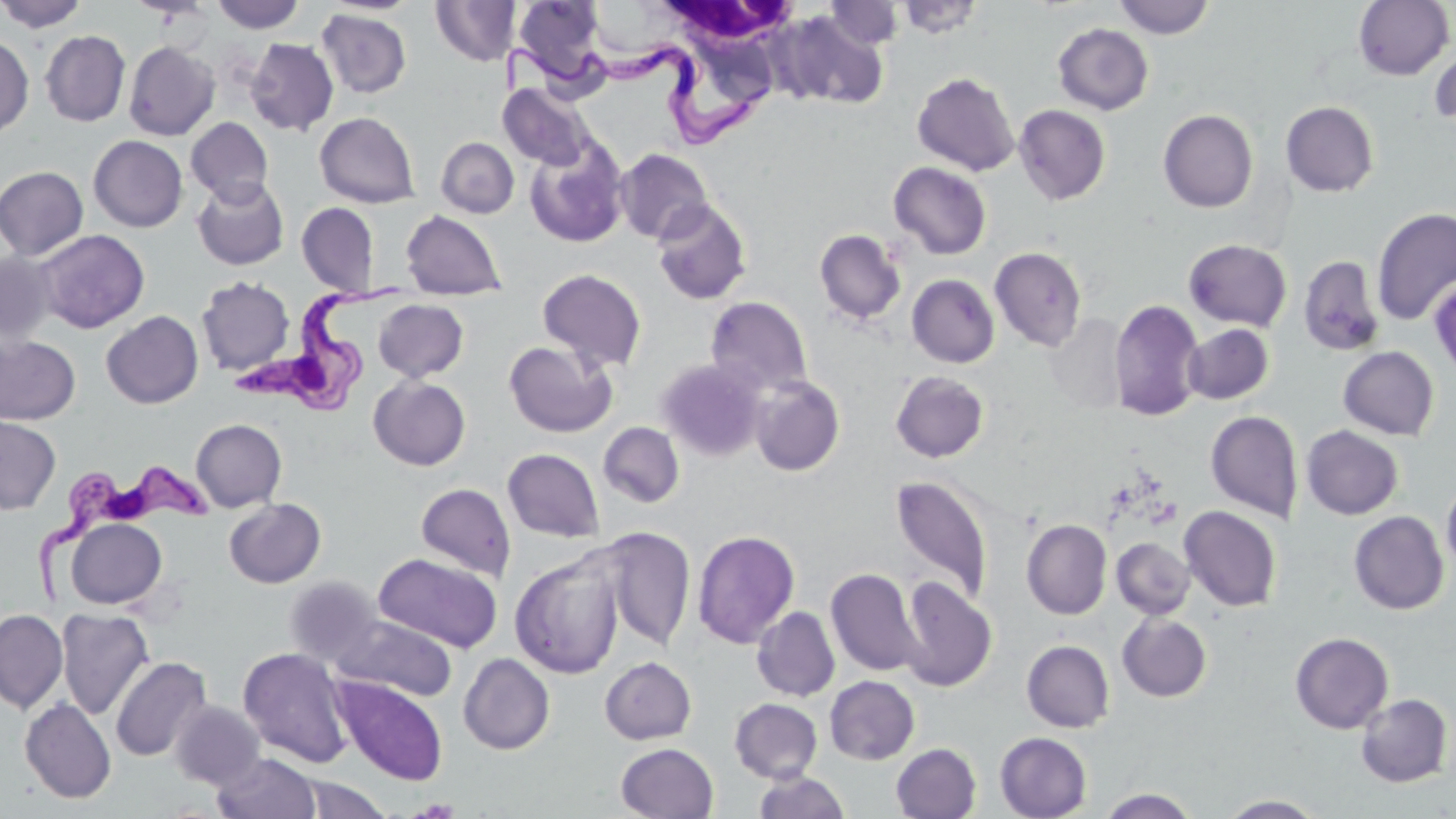
slide-level diagnosis = Trypanosoma brucei
modality = light microscopy
stain = May-Grünwald-Giemsa
Trypanosoma brucei locations = approximate bounding boxes as (x1, y1, x2, y2) in pixels: (501, 41, 779, 149), (232, 270, 406, 422), (31, 463, 218, 608)
field of view = single
white blood cell locations = approximate bounding boxes as (x1, y1, x2, y2) in pixels: (659, 1, 800, 53)
uninfected red blood cell locations = approximate bounding boxes as (x1, y1, x2, y2) in pixels: (0, 0, 88, 32), (211, 0, 305, 33), (513, 0, 607, 87), (585, 0, 679, 61), (895, 0, 985, 39), (1112, 0, 1215, 39), (1353, 0, 1454, 80), (320, 1, 422, 16), (431, 1, 516, 66), (822, 2, 905, 50), (316, 9, 412, 99), (775, 10, 889, 110), (1053, 23, 1154, 115), (40, 30, 130, 126), (0, 35, 34, 138), (245, 38, 339, 136), (124, 41, 220, 140), (1430, 42, 1456, 128), (912, 71, 1020, 176), (498, 83, 594, 170), (1281, 101, 1379, 197), (1014, 104, 1111, 205), (1158, 109, 1258, 213), (315, 112, 420, 208), (186, 117, 273, 205), (88, 135, 188, 232), (524, 135, 629, 249), (436, 137, 519, 218), (614, 148, 714, 244), (888, 162, 992, 260), (0, 166, 88, 260), (192, 178, 289, 270), (651, 198, 753, 306), (296, 202, 379, 297), (1372, 208, 1456, 326), (400, 209, 507, 300), (814, 228, 907, 326), (35, 229, 149, 332), (1184, 239, 1292, 331), (989, 247, 1087, 351), (0, 252, 58, 345), (1298, 255, 1385, 356), (536, 268, 647, 372), (907, 274, 999, 368), (196, 276, 295, 375), (1430, 276, 1456, 378), (706, 296, 813, 398), (374, 299, 469, 382), (1109, 299, 1204, 421), (101, 310, 203, 408), (1045, 313, 1129, 414), (1183, 324, 1274, 404), (0, 335, 80, 425), (504, 340, 617, 438), (1338, 346, 1439, 440), (657, 359, 768, 461), (891, 371, 989, 462), (369, 376, 471, 470), (749, 376, 845, 476), (1205, 411, 1303, 522), (0, 415, 61, 514), (191, 419, 287, 512), (598, 421, 685, 508), (1301, 425, 1404, 520), (502, 448, 604, 542), (890, 474, 994, 606), (1441, 478, 1456, 576), (416, 483, 516, 580), (224, 498, 326, 588), (1179, 506, 1282, 612), (1349, 510, 1449, 615), (64, 518, 167, 609), (1021, 519, 1112, 619), (596, 526, 696, 651), (692, 529, 800, 649), (1112, 538, 1195, 619), (509, 551, 625, 679), (373, 552, 503, 652), (825, 567, 925, 677), (284, 576, 382, 667), (898, 576, 997, 692), (752, 607, 840, 701), (56, 608, 154, 720), (0, 609, 68, 713), (1117, 614, 1212, 702), (333, 615, 458, 702), (1290, 632, 1394, 733), (1022, 640, 1114, 732), (238, 647, 353, 767), (458, 653, 555, 754), (599, 656, 696, 744), (110, 657, 211, 762), (332, 675, 448, 785), (824, 675, 920, 764), (1355, 694, 1453, 788), (20, 698, 116, 803), (730, 698, 823, 783), (169, 700, 265, 790), (995, 732, 1092, 819), (616, 742, 719, 819), (891, 743, 981, 819), (212, 753, 321, 819), (753, 771, 850, 819), (297, 775, 393, 818), (1097, 788, 1199, 818), (1218, 795, 1326, 818)
image size = 1456×819 pixels
preparation = thin blood film
magnification = 1000x